Give the extent of all Plasmodium ovale-infected red blood cells.
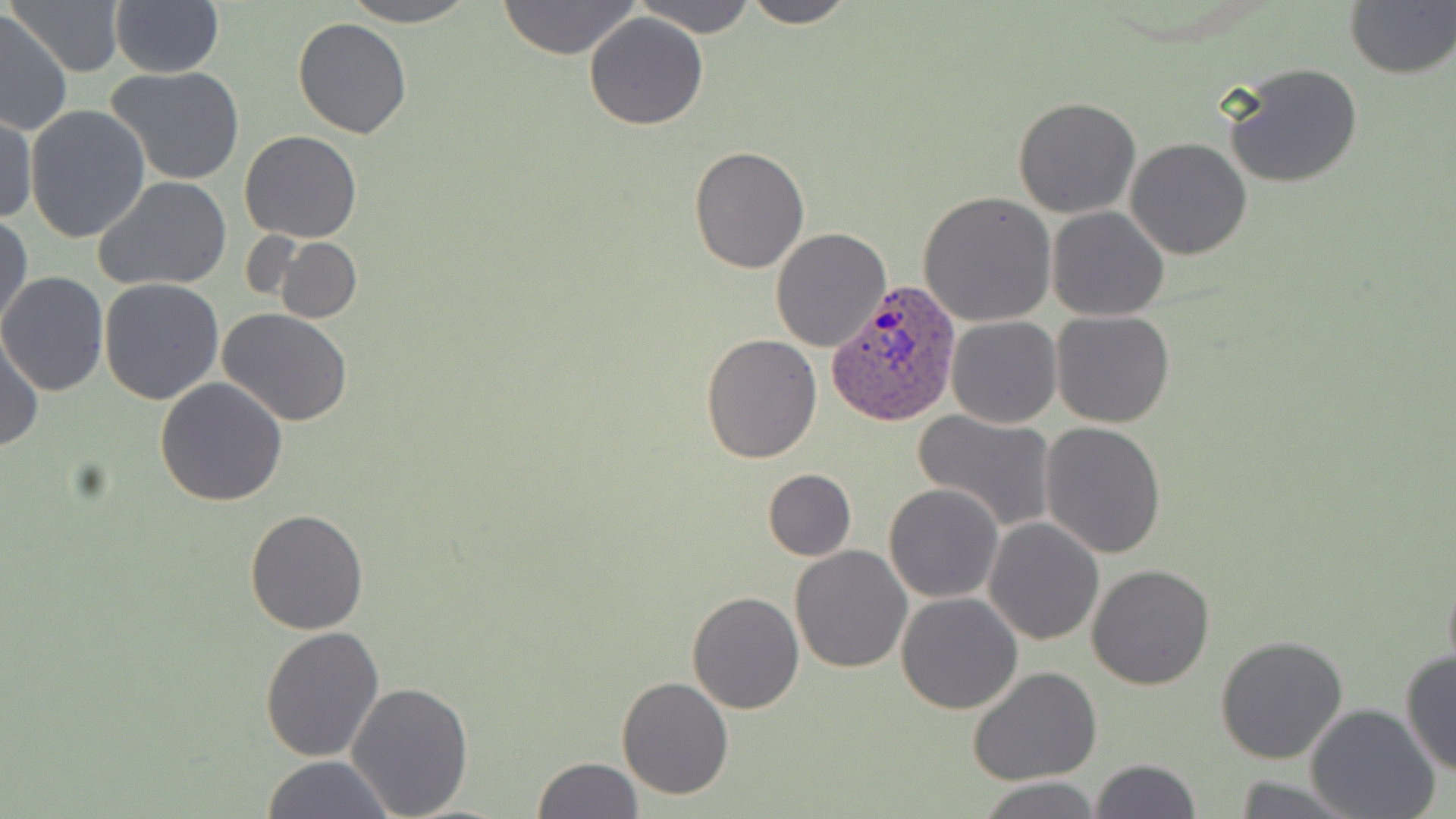

Approximate bounding boxes as (x1, y1, x2, y2) in pixels.
Plasmodium ovale-infected red blood cells: (828, 280, 961, 427).

slide-level diagnosis = Plasmodium ovale
field of view = one of a larger specimen
image size = 1456×819 pixels
stain = May-Grünwald-Giemsa
modality = light microscopy
magnification = 1000x
uninfected red blood cell locations = approximate bounding boxes as (x1, y1, x2, y2) in pixels: (6, 0, 128, 77), (109, 0, 224, 77), (339, 0, 480, 26), (495, 0, 643, 59), (633, 0, 758, 36), (739, 0, 856, 27), (1343, 0, 1455, 79), (1, 12, 71, 134), (583, 12, 708, 130), (293, 17, 412, 139), (1221, 61, 1364, 188), (107, 65, 245, 186), (1012, 97, 1142, 219), (25, 105, 151, 243), (0, 111, 36, 225), (239, 130, 363, 243), (1125, 137, 1253, 259), (688, 146, 810, 274), (94, 175, 232, 291), (918, 190, 1058, 326), (1047, 206, 1168, 321), (1, 213, 33, 335), (770, 228, 889, 351), (272, 236, 362, 325), (0, 273, 108, 396), (98, 278, 225, 405), (218, 308, 352, 427), (1050, 310, 1177, 428), (944, 316, 1062, 429), (1, 330, 44, 453), (700, 332, 822, 464), (153, 375, 288, 506), (913, 410, 1057, 533), (1039, 420, 1167, 558), (763, 469, 856, 560), (883, 482, 1004, 603), (245, 509, 369, 635), (984, 517, 1104, 645), (789, 546, 912, 673), (1442, 562, 1456, 682), (1086, 563, 1215, 688), (687, 591, 805, 714), (897, 591, 1022, 714), (259, 626, 385, 763), (1216, 633, 1350, 764), (1399, 651, 1455, 777), (968, 666, 1101, 784), (616, 676, 733, 800), (346, 682, 474, 816), (1305, 705, 1442, 818), (261, 756, 396, 818), (533, 757, 643, 818), (1087, 758, 1201, 819), (1227, 776, 1367, 816), (978, 777, 1104, 818)
preparation = thin blood film